Identify the parasite.
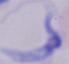

This is a trypanosome.

Micrograph. 1000x magnification.